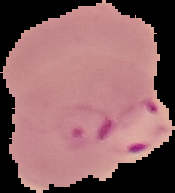 Image is 175×193 pixels. Cell region segmented out of the field of view; the surrounding area is masked to black. From a thin blood film. Malaria status: parasitized.